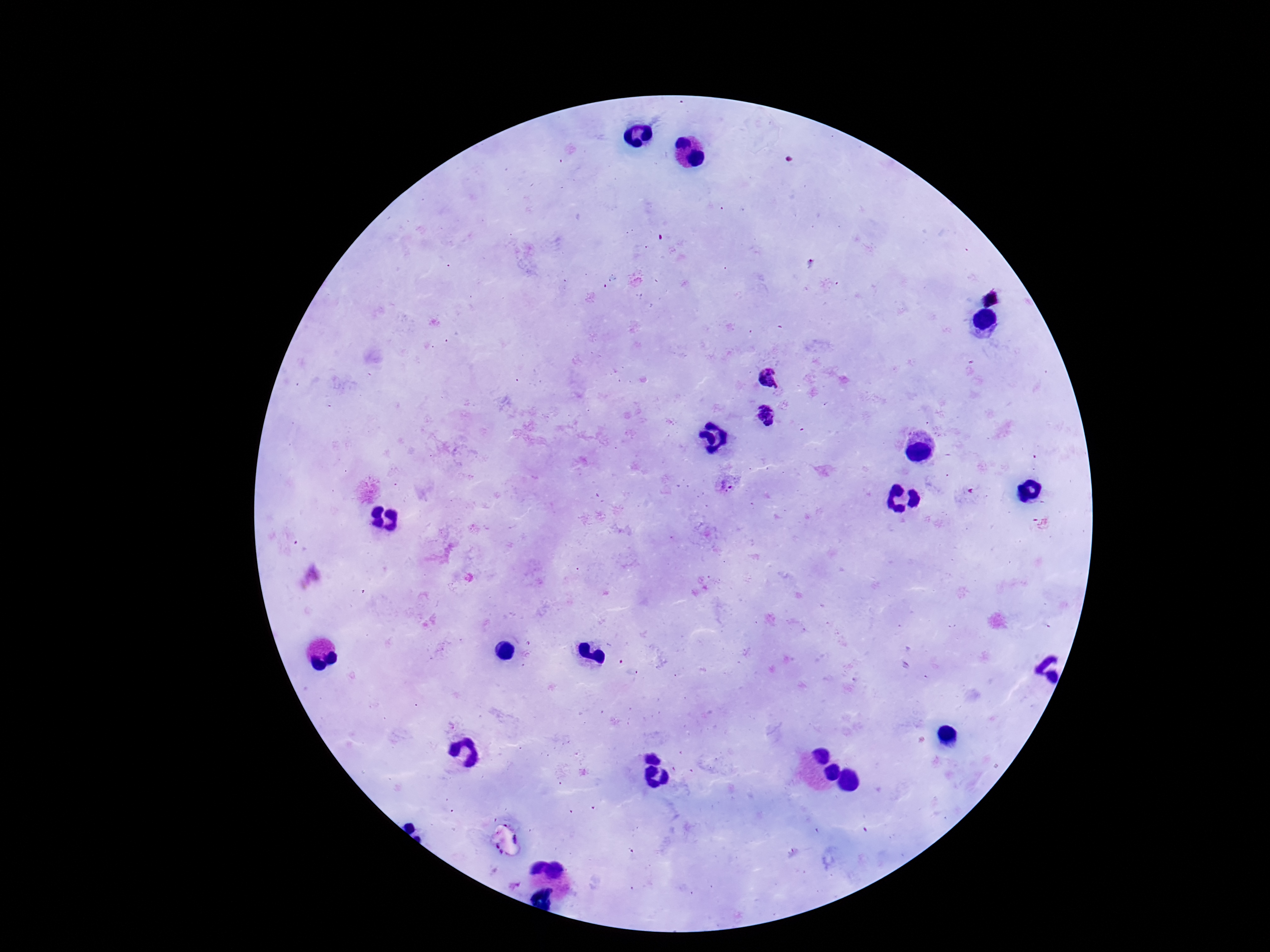
patient malaria status = positive
stain = Giemsa
magnification = 100x
Plasmodium parasite locations = approximate centers as [x, y] in pixels: [769, 379], [766, 416], [729, 485]
capture = smartphone camera through the microscope eyepiece
field of view = one from this slide
image size = 1270×952 pixels
preparation = thick blood smear